Give the position of every malaria parasite.
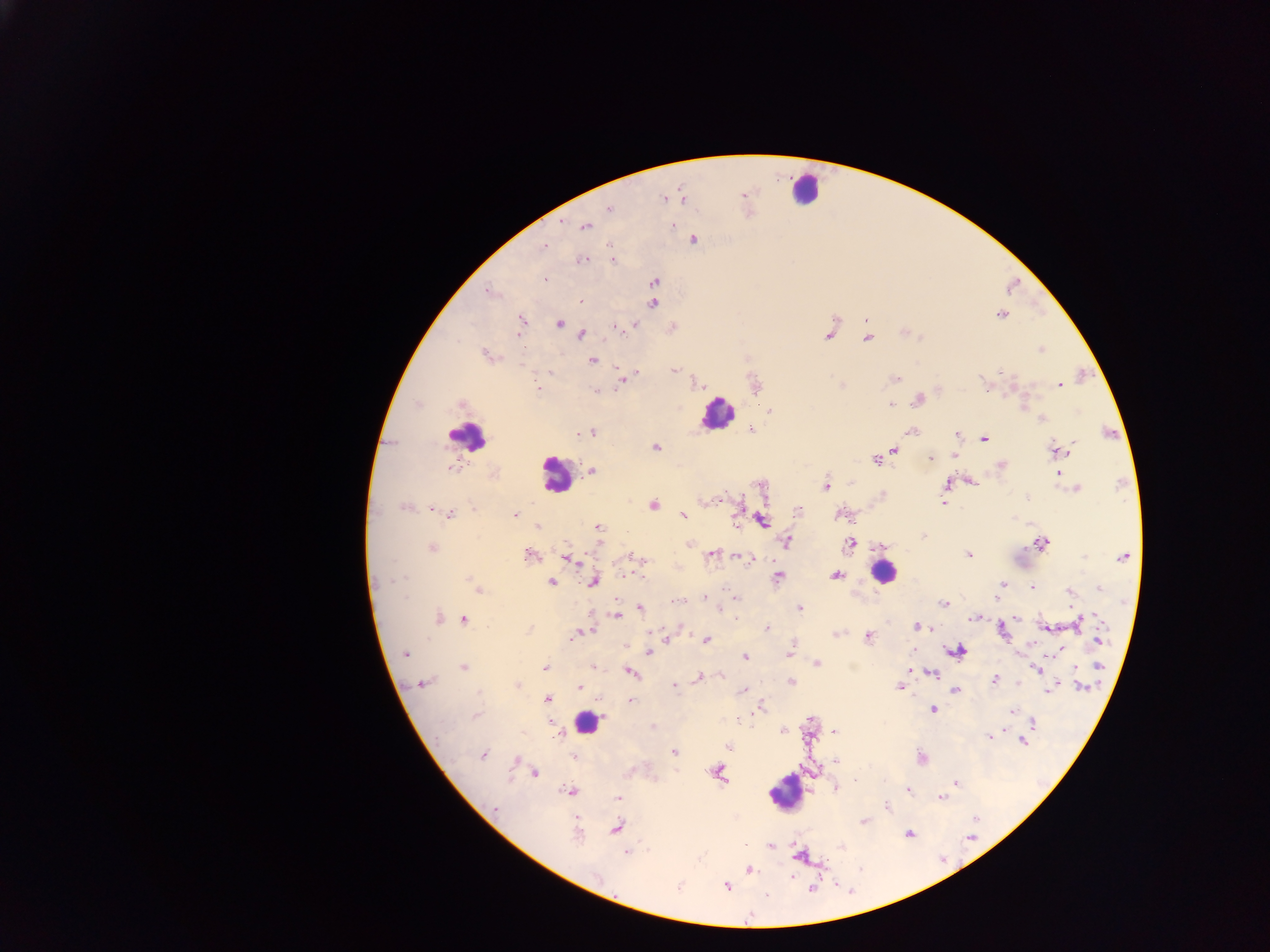
Approximate centers as (x, y) in pixels.
Malaria parasites: (742, 194), (683, 198), (663, 199), (610, 209), (561, 221), (672, 226), (585, 227), (694, 240), (545, 246), (582, 260), (613, 260), (546, 279), (654, 282), (489, 293), (581, 302), (653, 303), (1001, 314), (866, 319), (521, 321), (560, 324), (634, 325), (616, 327), (519, 332), (581, 334), (829, 335), (868, 338), (1041, 349), (486, 355), (592, 360), (674, 370), (550, 372), (637, 374), (895, 378), (623, 379), (985, 384), (842, 385), (1059, 385), (539, 388), (596, 391), (918, 400), (460, 404), (890, 404), (1023, 407), (771, 410), (1042, 419), (751, 429), (912, 431), (581, 433), (591, 433), (957, 435), (983, 439), (654, 447), (894, 449), (1058, 450), (956, 454), (884, 455), (930, 458), (875, 460), (1001, 465), (450, 468), (592, 470), (1058, 474), (972, 481), (947, 483), (826, 485), (1077, 488), (883, 495), (716, 499), (944, 504), (654, 506), (405, 507), (434, 509), (473, 509), (798, 511), (450, 514), (515, 514), (683, 515), (841, 515), (762, 520), (538, 526), (598, 527), (923, 536), (849, 542), (785, 543), (1042, 543), (688, 544), (432, 548), (712, 554), (968, 555), (529, 556), (741, 556), (1123, 557), (635, 559), (747, 559), (573, 560), (836, 575), (778, 577), (398, 579), (472, 581), (594, 581), (551, 582), (1003, 583), (1099, 587), (1032, 588), (478, 589), (1070, 591), (732, 595), (995, 597), (705, 598), (678, 601), (944, 604), (640, 608), (719, 608), (800, 608), (616, 616), (1016, 617), (438, 618), (975, 618), (463, 619), (1078, 623), (917, 627), (1045, 627), (767, 628), (528, 630), (585, 632), (1003, 633), (580, 634), (837, 634), (572, 636), (869, 637), (667, 639), (706, 639), (1100, 641), (958, 651), (1058, 651), (648, 652), (790, 652), (405, 653), (745, 657), (816, 663), (593, 666), (1099, 666), (463, 667), (545, 667), (1036, 669), (910, 670), (630, 673), (930, 674), (720, 675), (699, 678), (995, 680), (791, 683), (424, 684), (517, 685), (675, 685), (899, 687), (1054, 687), (1083, 687), (580, 688), (1049, 689), (743, 690), (956, 690), (547, 699), (630, 700), (760, 708), (932, 709), (1011, 712), (476, 716), (551, 723), (1032, 723), (783, 730), (835, 732), (989, 736), (1022, 741), (728, 747), (673, 752), (483, 755), (573, 757), (922, 759), (516, 761), (837, 762), (536, 772), (718, 774), (855, 780), (955, 783), (836, 787), (569, 791), (908, 791), (942, 797), (618, 798), (886, 806), (495, 810), (975, 818), (864, 822), (617, 827), (577, 833), (909, 833), (770, 845), (627, 853), (799, 857), (749, 870), (597, 876), (790, 877), (726, 887), (813, 889), (766, 895).

Leukocyte locations: (805, 188), (716, 413), (466, 436), (555, 474), (883, 572), (587, 723), (784, 793). Sample from Ghana. Thick blood film. Image is 1270×952 pixels. Single field of view. Photographed through a microscope with a mobile-phone camera.